Locate and identify every blood parasite.
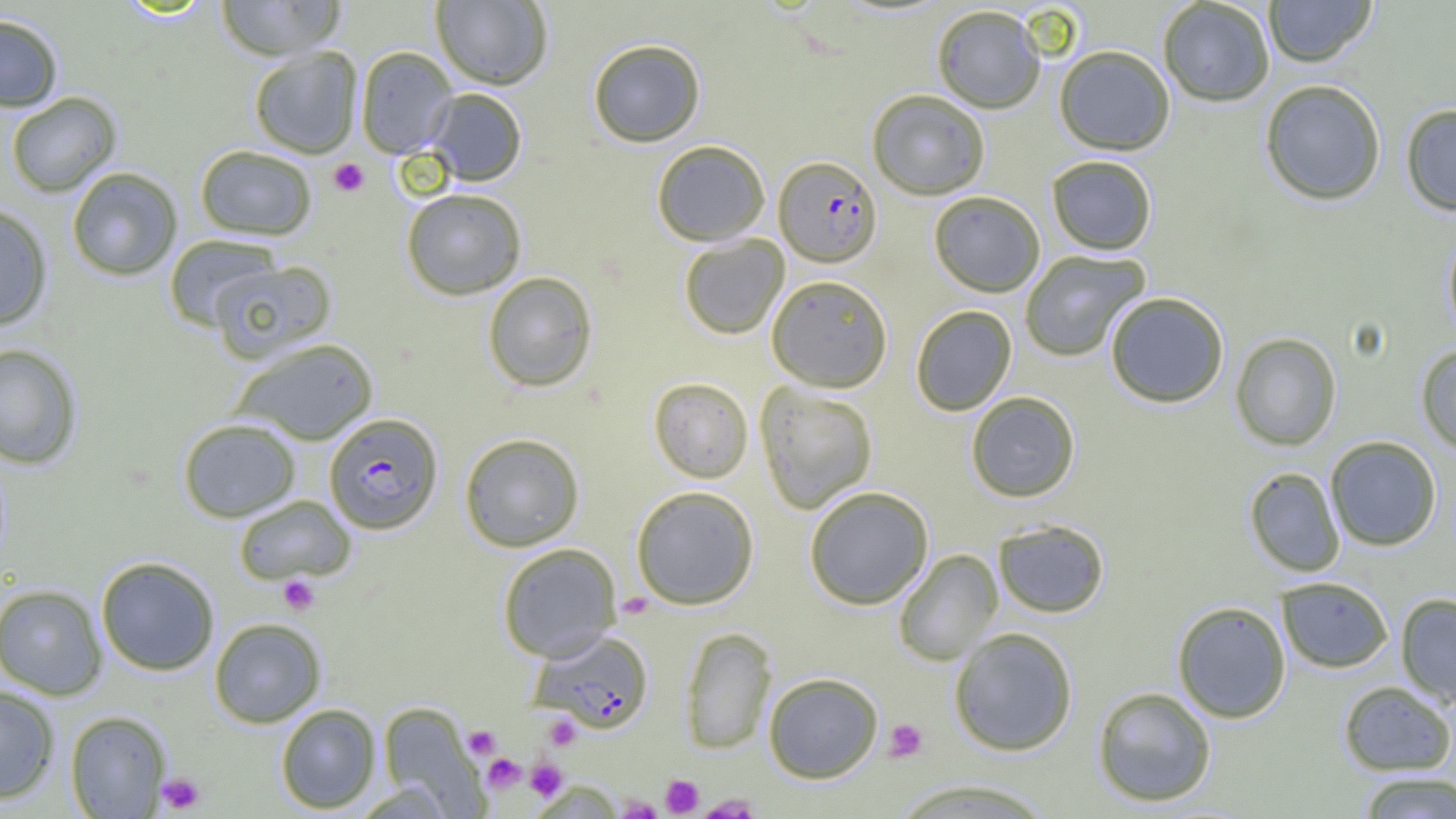
Approximate bounding boxes as named x1/y1/x2/y2 corners in pixels.
Plasmodium falciparum-infected red blood cells: (x1=774, y1=156, x2=881, y2=267), (x1=324, y1=413, x2=443, y2=534), (x1=529, y1=630, x2=654, y2=733).
No Plasmodium ovale, Plasmodium malariae, Plasmodium vivax, Babesia divergens, or Trypanosoma brucei observed.

{
  "slide_level_diagnosis": "Plasmodium falciparum",
  "uninfected_red_blood_cell_locations_subset": "approximate bounding boxes as named x1/y1/x2/y2 corners in pixels: (x1=214, y1=0, x2=346, y2=60), (x1=431, y1=0, x2=553, y2=90), (x1=1157, y1=0, x2=1275, y2=107), (x1=1263, y1=0, x2=1377, y2=67), (x1=931, y1=5, x2=1046, y2=113), (x1=0, y1=14, x2=63, y2=112), (x1=588, y1=39, x2=706, y2=146), (x1=1054, y1=45, x2=1175, y2=155), (x1=355, y1=46, x2=457, y2=158), (x1=248, y1=47, x2=363, y2=158), (x1=1259, y1=79, x2=1387, y2=205), (x1=426, y1=88, x2=527, y2=186), (x1=867, y1=89, x2=990, y2=200), (x1=6, y1=91, x2=122, y2=197), (x1=1400, y1=103, x2=1456, y2=216), (x1=651, y1=140, x2=770, y2=246), (x1=195, y1=145, x2=318, y2=241), (x1=1047, y1=155, x2=1157, y2=255), (x1=66, y1=167, x2=182, y2=281), (x1=401, y1=188, x2=527, y2=300), (x1=928, y1=190, x2=1045, y2=296), (x1=0, y1=203, x2=53, y2=331), (x1=1442, y1=225, x2=1456, y2=343), (x1=163, y1=234, x2=283, y2=332), (x1=678, y1=234, x2=789, y2=339), (x1=1019, y1=250, x2=1151, y2=362), (x1=210, y1=260, x2=336, y2=364), (x1=483, y1=271, x2=598, y2=392), (x1=766, y1=274, x2=893, y2=392), (x1=1104, y1=291, x2=1229, y2=408), (x1=911, y1=305, x2=1017, y2=416), (x1=1230, y1=332, x2=1342, y2=451), (x1=231, y1=338, x2=379, y2=445), (x1=0, y1=343, x2=83, y2=469), (x1=1415, y1=344, x2=1456, y2=454), (x1=648, y1=377, x2=754, y2=483), (x1=755, y1=382, x2=878, y2=514), (x1=966, y1=391, x2=1081, y2=502), (x1=177, y1=417, x2=301, y2=522), (x1=459, y1=432, x2=585, y2=552), (x1=1325, y1=436, x2=1442, y2=551), (x1=1244, y1=467, x2=1345, y2=577), (x1=631, y1=485, x2=760, y2=610), (x1=804, y1=485, x2=934, y2=610), (x1=233, y1=495, x2=356, y2=585), (x1=993, y1=518, x2=1110, y2=618), (x1=497, y1=542, x2=622, y2=662), (x1=893, y1=549, x2=1003, y2=666), (x1=95, y1=556, x2=220, y2=676), (x1=1276, y1=577, x2=1394, y2=673), (x1=0, y1=583, x2=108, y2=700), (x1=1395, y1=593, x2=1456, y2=708), (x1=1172, y1=601, x2=1292, y2=723), (x1=209, y1=617, x2=326, y2=728), (x1=679, y1=627, x2=776, y2=754), (x1=948, y1=627, x2=1079, y2=756), (x1=763, y1=672, x2=883, y2=783), (x1=1338, y1=680, x2=1456, y2=775), (x1=0, y1=685, x2=60, y2=804), (x1=1092, y1=686, x2=1217, y2=807), (x1=275, y1=703, x2=381, y2=813), (x1=65, y1=710, x2=171, y2=818), (x1=1356, y1=771, x2=1456, y2=818), (x1=889, y1=777, x2=1058, y2=818)",
  "magnification": "1000x",
  "field_of_view": "single",
  "modality": "light microscopy",
  "preparation": "thin blood smear",
  "platelet_locations_subset": "approximate bounding boxes as named x1/y1/x2/y2 corners in pixels: (x1=328, y1=158, x2=369, y2=197), (x1=278, y1=575, x2=320, y2=615), (x1=543, y1=715, x2=581, y2=750), (x1=884, y1=718, x2=929, y2=762), (x1=463, y1=725, x2=501, y2=759), (x1=482, y1=753, x2=526, y2=794), (x1=526, y1=759, x2=567, y2=801), (x1=156, y1=772, x2=206, y2=814), (x1=661, y1=774, x2=704, y2=817), (x1=617, y1=796, x2=661, y2=819), (x1=697, y1=796, x2=763, y2=818)",
  "image_size": "1456×819 pixels"
}